Describe the morphology of the red blood cells.
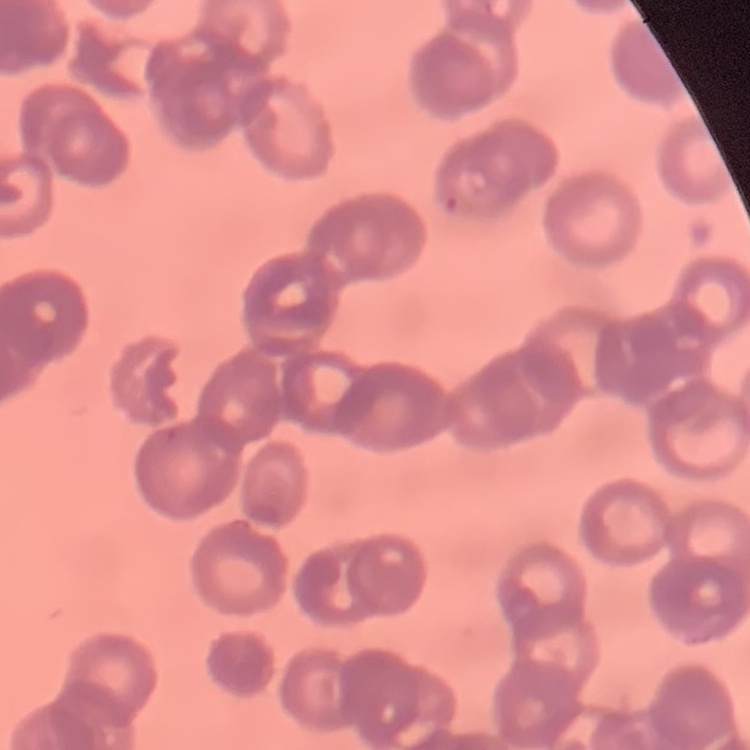

They show rouleaux formation.

{
  "stain": "Field's or Giemsa",
  "preparation": "thin blood smear",
  "image_type": "square crop of a larger photomicrograph"
}